Report the malaria status of this cell.
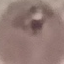

It is parasitized.

Summary:
  - Stain: Giemsa
  - Image type: cell patch, automatically extracted from a larger field of view and resized to 64 × 64 pixels
  - Preparation: thin blood smear
  - Capture: smartphone through the microscope eyepiece